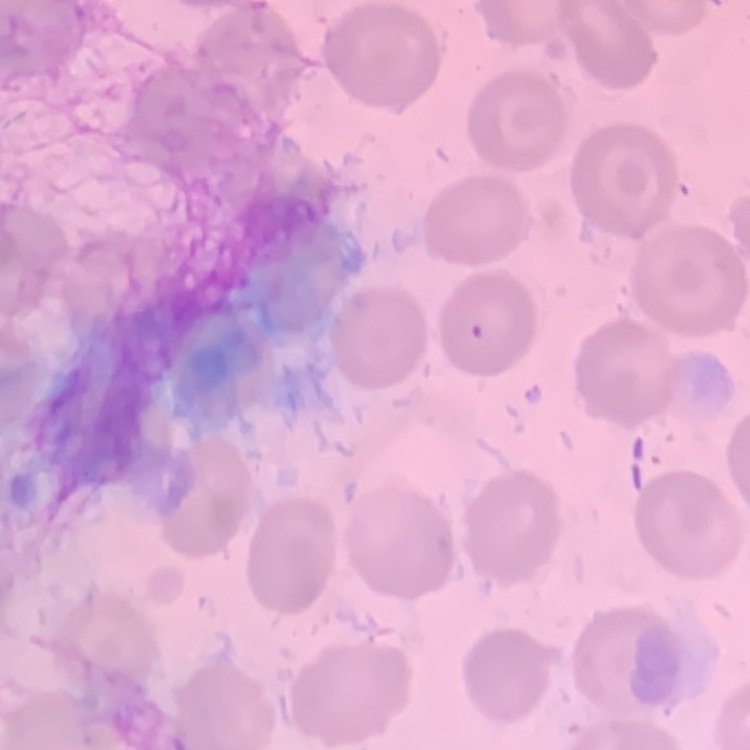
The erythrocytes show no rouleaux formation. Stained with either Field's or Giemsa. Thin blood film. Square crop of a larger photomicrograph.